Classify this cell by malaria status.
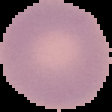

Uninfected.

Summary:
  - Image type: cell region segmented out of the field of view; surrounding area masked to black
  - Image size: 112×112 pixels
  - Preparation: thin blood film